Classify this cell by malaria status.
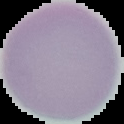
Uninfected.

The area outside the segmented cell region is set to black. Image is 124×124 pixels. From a thin blood smear.